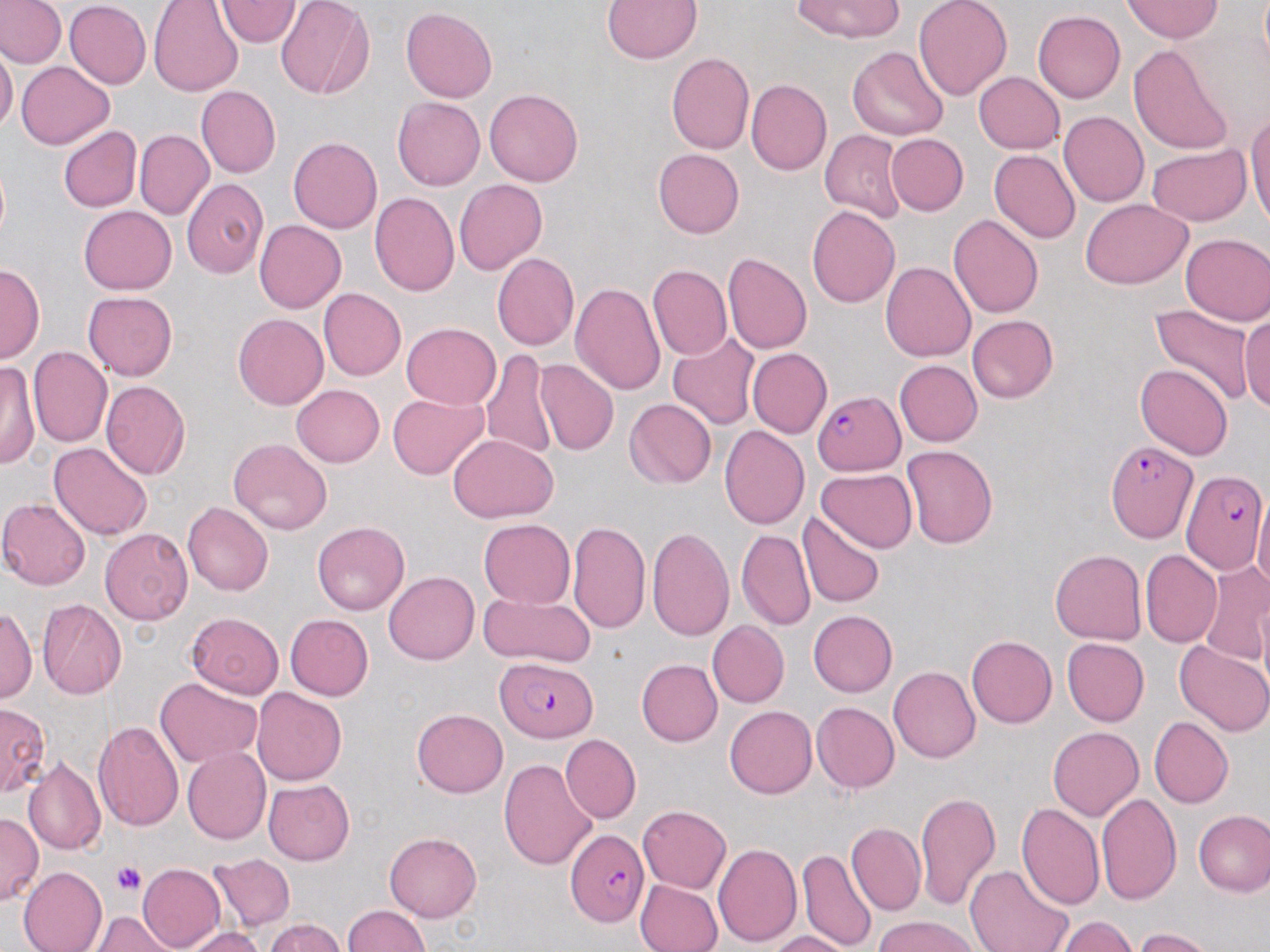 Approximate bounding boxes as (x1,y1)-(x2,y2) corner pairs in pixels. Platelet locations: (111,861)-(147,895). Uninfected red blood cell locations: (0,0)-(65,67), (215,0)-(302,48), (602,0)-(702,64), (791,0)-(903,43), (65,1)-(151,89), (913,1)-(1012,103), (1122,1)-(1222,42), (150,2)-(243,99), (275,2)-(374,102), (401,7)-(497,103), (1034,11)-(1125,103), (1127,43)-(1237,156), (0,44)-(18,134), (846,46)-(949,139), (666,53)-(754,154), (16,61)-(114,150), (973,72)-(1064,154), (746,80)-(831,176), (197,84)-(281,178), (484,88)-(584,187), (393,97)-(485,190), (1246,109)-(1270,235), (1059,111)-(1149,208), (57,125)-(141,212), (135,130)-(213,219), (820,130)-(906,223), (885,133)-(968,217), (289,137)-(382,234), (1147,145)-(1251,226), (652,148)-(744,239), (988,149)-(1081,243), (181,178)-(268,278), (454,179)-(548,276), (370,192)-(460,295), (1082,199)-(1194,288), (79,206)-(176,294), (806,206)-(900,309), (948,215)-(1043,318), (254,219)-(346,313), (1180,234)-(1270,325), (889,242)-(1029,347), (493,253)-(579,351), (722,253)-(811,355), (0,262)-(45,363), (880,262)-(975,361), (647,265)-(732,360), (570,283)-(666,396), (318,288)-(406,381), (83,292)-(177,381), (1147,304)-(1257,409), (233,313)-(329,410), (1239,313)-(1269,412), (966,315)-(1058,404), (401,323)-(500,409), (667,331)-(760,430), (28,347)-(112,448), (747,348)-(831,438), (481,349)-(557,460), (535,358)-(618,456), (895,360)-(983,446), (1,362)-(37,471), (1135,363)-(1233,460), (100,380)-(190,480), (292,385)-(384,467), (387,393)-(488,480), (625,398)-(716,489), (719,425)-(809,529), (448,434)-(558,523), (228,438)-(332,535), (49,442)-(152,539), (901,445)-(997,548), (815,469)-(918,553), (1253,496)-(1270,593), (0,497)-(91,590), (183,502)-(273,596), (796,512)-(886,609), (479,519)-(575,608), (568,521)-(651,633), (312,522)-(409,614), (99,527)-(193,625), (646,527)-(734,640), (735,530)-(814,631), (1049,549)-(1147,645), (1140,550)-(1220,647), (1199,560)-(1270,666), (384,571)-(479,665), (478,589)-(595,667), (37,598)-(126,700), (0,605)-(37,703), (808,610)-(898,697), (185,611)-(283,699), (285,614)-(373,701), (708,621)-(790,707), (966,635)-(1057,728), (1062,637)-(1149,726), (1173,641)-(1270,737), (636,659)-(721,746), (888,666)-(980,763), (156,677)-(263,767), (252,688)-(346,785), (812,702)-(899,792), (0,704)-(52,797), (725,705)-(818,798), (411,709)-(508,798), (1149,716)-(1233,808), (92,721)-(184,831), (1048,727)-(1143,820), (560,735)-(640,823), (182,747)-(271,845), (22,756)-(106,855), (499,759)-(597,871), (263,778)-(354,865), (914,791)-(1000,912), (1095,791)-(1182,906), (1016,802)-(1104,910), (637,805)-(731,893), (1194,810)-(1270,896), (0,813)-(42,906), (847,823)-(925,915), (384,832)-(482,922), (712,843)-(802,947), (796,849)-(877,951), (208,853)-(295,932), (136,863)-(224,952), (963,864)-(1075,952), (18,867)-(108,952), (635,878)-(723,952), (343,904)-(428,952), (89,912)-(179,952), (874,916)-(979,952), (1052,916)-(1137,952), (264,918)-(346,951), (181,927)-(267,952), (1133,928)-(1220,952), (768,930)-(854,951). Plasmodium falciparum-infected red blood cell locations: (813,389)-(905,476), (1105,438)-(1199,546), (1180,470)-(1265,576), (498,658)-(597,742), (567,828)-(650,926). Slide-level diagnosis: Plasmodium falciparum. May-Grünwald-Giemsa stain. Captured at 1000x magnification. Thin blood film. Optical microscopy. Image is 1270×952 pixels. One field of a larger specimen.